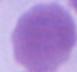

{
  "identification": "red blood cell",
  "modality": "photomicrograph",
  "magnification": "1000x"
}